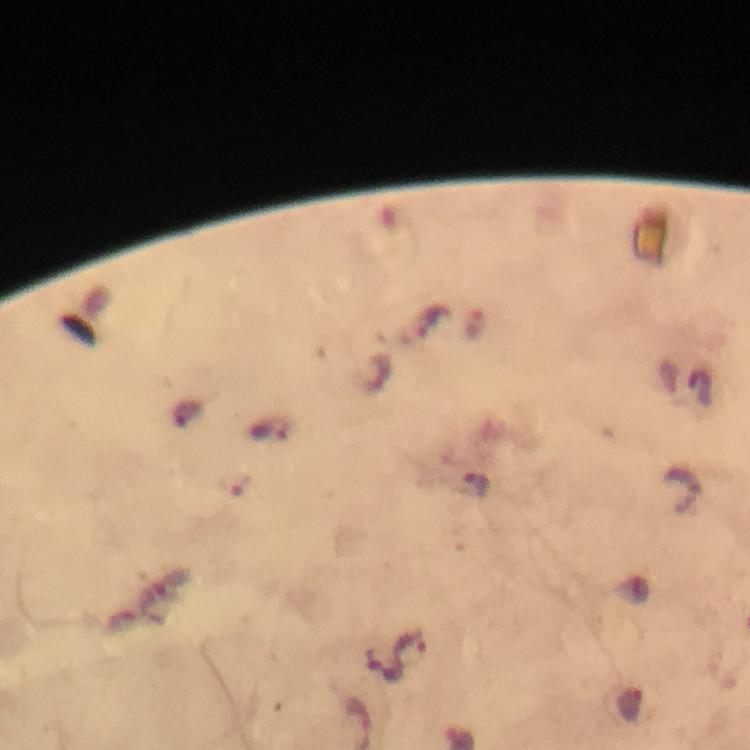
context: from a diagnostic examination for malaria
capture: smartphone mounted on the microscope
preparation: thick smear
stain: Giemsa
magnification: 100x
malaria_parasite_locations: 'approximate centers as [x, y] in pixels: [430, 322], [375, 372], [271, 430], [476, 488], [685, 491], [410, 649]'
immersion_oil: used
cropped_from: one field of view
image_size: 750×750 pixels